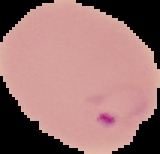
Summary:
  - Result: Plasmodium parasites identified
  - Preparation: thin blood film
  - Image size: 160×154 pixels
  - Image type: segmented cell region with the area outside set to black